Classify this cell by malaria status.
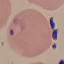

Parasitized.

Summary:
  - Preparation: thin blood smear
  - Capture: smartphone through the microscope eyepiece
  - Image type: automatically extracted cell patch, resized to 64 × 64 pixels
  - Stain: Giemsa